Identify the blood parasite species.
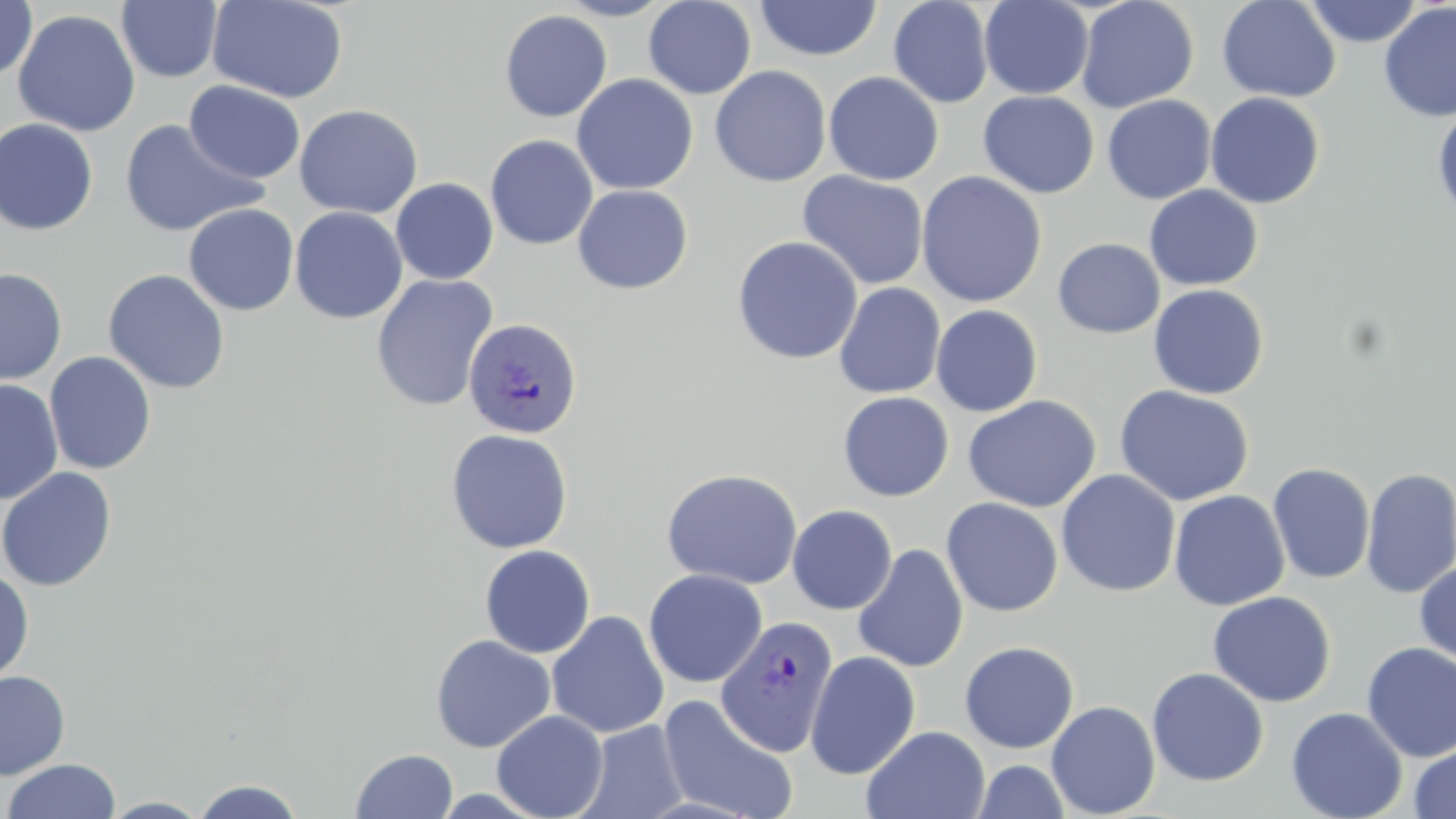

Plasmodium vivax.

Approximate bounding boxes as [x1, y1, x2, y2] in pixels. Uninfected red blood cell locations: [0, 0, 36, 82], [209, 0, 348, 103], [554, 0, 675, 20], [643, 0, 756, 99], [1075, 0, 1199, 113], [1216, 0, 1341, 103], [1303, 0, 1423, 47], [117, 1, 223, 83], [755, 1, 881, 61], [888, 1, 994, 108], [979, 1, 1093, 100], [1378, 2, 1456, 122], [12, 9, 140, 137], [499, 10, 613, 122], [710, 66, 832, 187], [823, 71, 944, 186], [571, 74, 698, 195], [183, 80, 305, 183], [978, 91, 1099, 198], [1204, 92, 1325, 208], [1101, 95, 1217, 204], [1432, 103, 1456, 222], [294, 104, 424, 219], [0, 117, 99, 235], [119, 118, 264, 237], [485, 134, 598, 250], [797, 171, 930, 290], [915, 171, 1048, 308], [390, 178, 498, 284], [1144, 184, 1263, 291], [572, 185, 694, 295], [183, 203, 300, 316], [290, 206, 408, 324], [731, 236, 863, 365], [1052, 238, 1164, 338], [0, 267, 67, 385], [102, 269, 230, 394], [370, 274, 499, 412], [833, 283, 946, 399], [1148, 284, 1269, 399], [930, 304, 1043, 417], [43, 351, 157, 474], [0, 378, 64, 506], [1113, 385, 1255, 506], [838, 391, 954, 501], [963, 395, 1102, 513], [445, 428, 573, 554], [1267, 462, 1375, 584], [0, 467, 117, 592], [1360, 467, 1456, 599], [661, 468, 803, 590], [1056, 469, 1181, 597], [1168, 490, 1290, 611], [941, 497, 1063, 616], [787, 504, 898, 614], [853, 543, 969, 673], [479, 544, 596, 658], [1414, 561, 1456, 669], [0, 567, 34, 685], [643, 569, 767, 688], [1207, 590, 1336, 707], [546, 610, 669, 739], [430, 634, 556, 753], [959, 641, 1079, 753], [1361, 643, 1456, 762], [805, 651, 921, 780], [1146, 667, 1269, 787], [0, 670, 70, 780], [658, 694, 798, 819], [1046, 700, 1161, 817], [1286, 706, 1408, 819], [492, 710, 609, 819], [578, 720, 689, 819], [861, 725, 991, 819], [1409, 743, 1456, 819], [350, 748, 458, 819], [3, 758, 121, 818], [972, 759, 1071, 819], [190, 778, 307, 818], [99, 796, 213, 818]. Plasmodium vivax-infected red blood cell locations: [463, 317, 583, 440], [715, 616, 839, 757]. May-Grünwald-Giemsa-stained preparation. Single field of view. Optical microscopy. Captured at 1000x magnification. Image is 1456×819 pixels. Thin blood smear.